Classify this cell by malaria status.
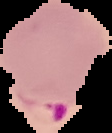
It is parasitized.

Summary:
  - Preparation: thin blood film
  - Image type: cell region segmented out of the field of view; surrounding area masked to black
  - Image size: 112×133 pixels